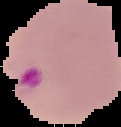
From a thin blood smear. Malaria status: parasitized. Cell region segmented out of the field of view; the surrounding area is masked to black. Image is 121×127 pixels.